Report the malaria status of this cell.
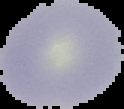
It is uninfected.

preparation = thin blood film
image size = 124×109 pixels
image type = segmented cell region on a black background